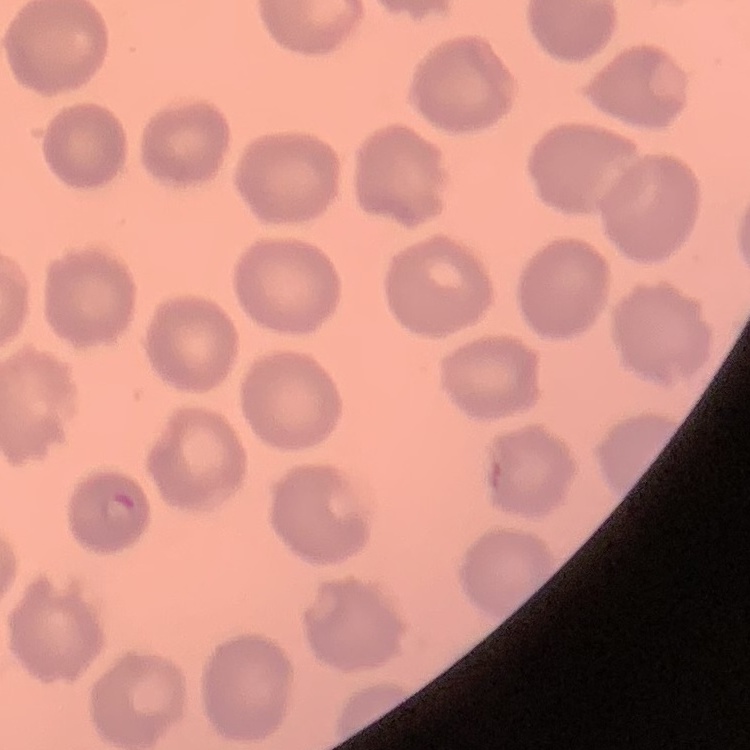

Summary:
  - Red blood cell morphology: no rouleaux formation
  - Image type: square crop of a larger photomicrograph
  - Preparation: thin peripheral smear
  - Stain: Field's or Giemsa